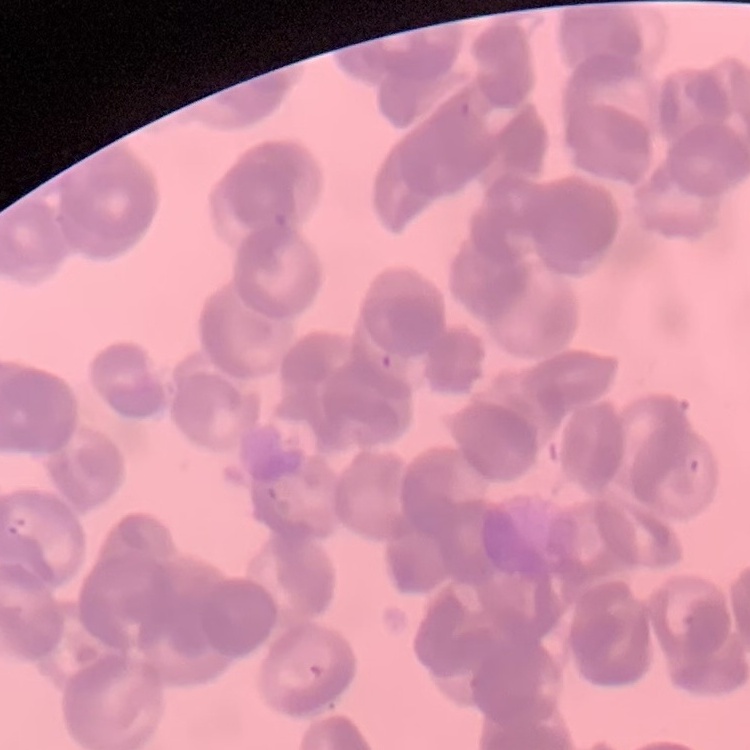

{
  "erythrocyte_morphology": "rouleaux formation",
  "image_type": "square crop of a larger photomicrograph",
  "stain": "Field's or Giemsa",
  "preparation": "thin peripheral smear"
}